Comment on the morphology of the erythrocytes.
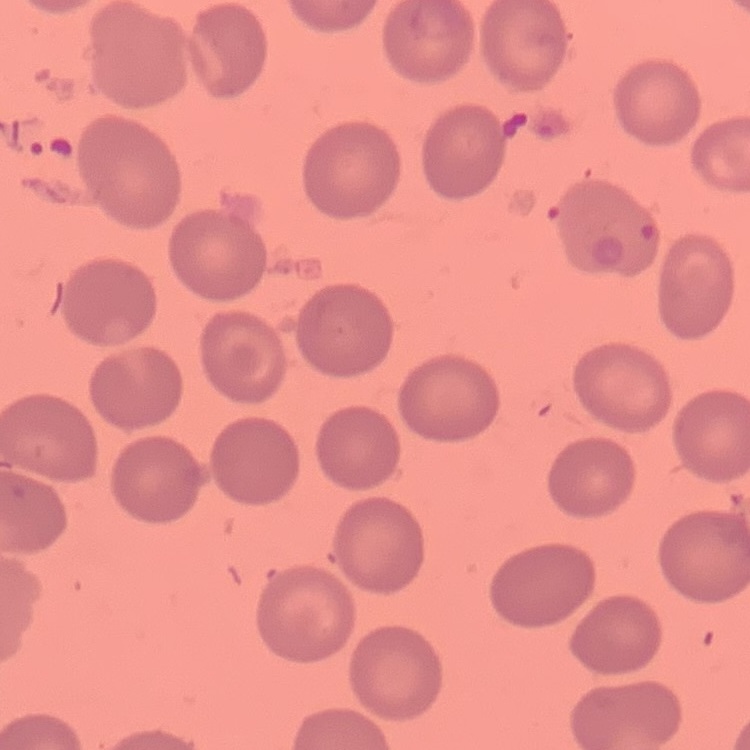

No rouleaux formation.

Square crop of a larger photomicrograph. Thin blood film. Stained with either Field's or Giemsa.